State the blood parasite species.
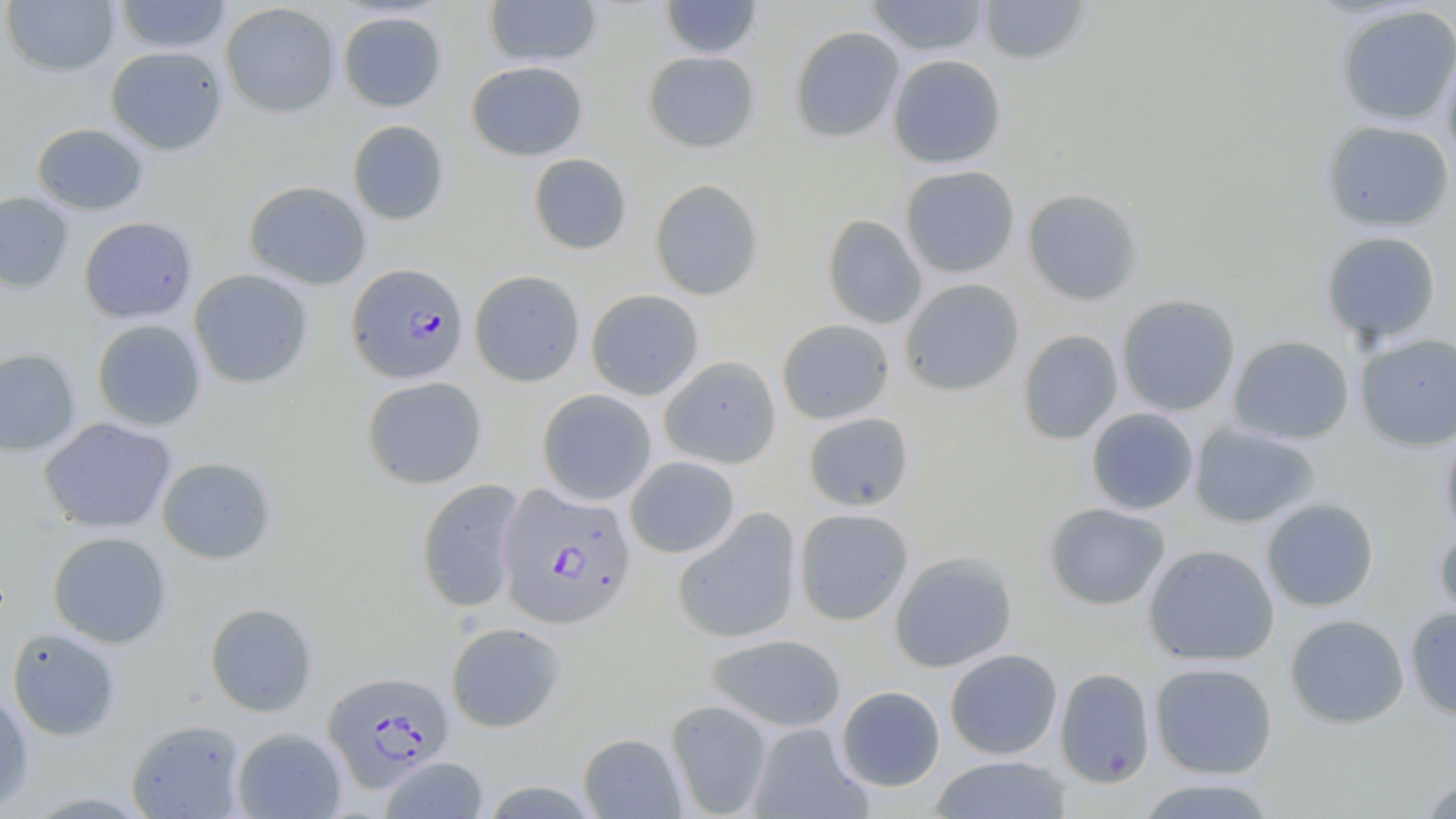
Plasmodium falciparum.

modality: light microscopy
preparation: thin blood film
field_of_view: one of a larger specimen
stain: May-Grünwald-Giemsa
plasmodium_falciparum_infected_red_blood_cell_locations: 'approximate bounding boxes as [x1, y1, x2, y2] in pixels: [347, 262, 469, 384], [496, 483, 636, 630], [323, 670, 454, 790]'
magnification: 1000x
uninfected_red_blood_cell_locations: 'approximate bounding boxes as [x1, y1, x2, y2] in pixels: [113, 0, 232, 53], [484, 0, 602, 67], [866, 0, 989, 57], [978, 0, 1091, 65], [2, 1, 119, 76], [660, 1, 763, 59], [220, 3, 340, 118], [1335, 4, 1456, 126], [337, 10, 447, 112], [789, 26, 905, 143], [796, 39, 996, 155], [105, 45, 227, 155], [1441, 48, 1456, 168], [643, 51, 760, 153], [887, 54, 1006, 169], [466, 60, 588, 161], [347, 120, 449, 225], [1322, 120, 1455, 231], [31, 123, 148, 215], [528, 153, 632, 255], [900, 165, 1020, 278], [649, 178, 765, 300], [244, 180, 371, 290], [1022, 188, 1145, 305], [0, 191, 73, 293], [822, 214, 926, 329], [79, 216, 197, 323], [1320, 231, 1442, 344], [188, 269, 313, 388], [469, 270, 585, 386], [900, 278, 1024, 396], [586, 289, 704, 400], [1116, 294, 1241, 416], [91, 319, 206, 431], [776, 319, 894, 424], [1018, 329, 1124, 445], [1355, 333, 1455, 450], [1228, 335, 1355, 445], [0, 348, 81, 457], [659, 355, 782, 469], [362, 376, 487, 489], [537, 389, 657, 505], [1085, 407, 1200, 514], [803, 411, 914, 511], [39, 417, 176, 533], [1190, 423, 1320, 528], [1440, 426, 1456, 541], [625, 456, 740, 558], [156, 457, 276, 564], [416, 479, 527, 614], [1261, 498, 1379, 611], [1044, 503, 1171, 611], [672, 507, 802, 644], [794, 508, 913, 625], [1434, 524, 1456, 631], [47, 531, 172, 648], [1143, 544, 1279, 666], [889, 551, 1018, 672], [204, 602, 318, 717], [1405, 607, 1456, 720], [1284, 613, 1410, 729], [446, 621, 566, 732], [7, 627, 121, 741], [706, 633, 847, 732], [944, 649, 1063, 760], [1149, 662, 1278, 779], [1054, 667, 1156, 788], [0, 684, 34, 815], [836, 685, 945, 791], [665, 699, 773, 818], [126, 718, 248, 818], [748, 723, 870, 818], [232, 727, 346, 818], [578, 733, 686, 819], [929, 755, 1072, 818], [378, 756, 489, 819], [1418, 775, 1456, 819], [1133, 777, 1278, 819]'
image_size: 1456×819 pixels